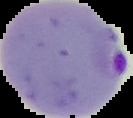
From a thin blood smear. Result: malaria parasites identified. Image is 133×118 pixels. Segmented cell region on a black background.